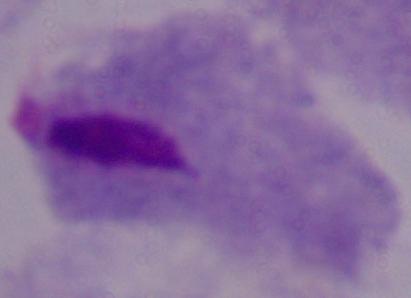 A trichomonad is seen. Photomicrograph. Captured at 1000x magnification.